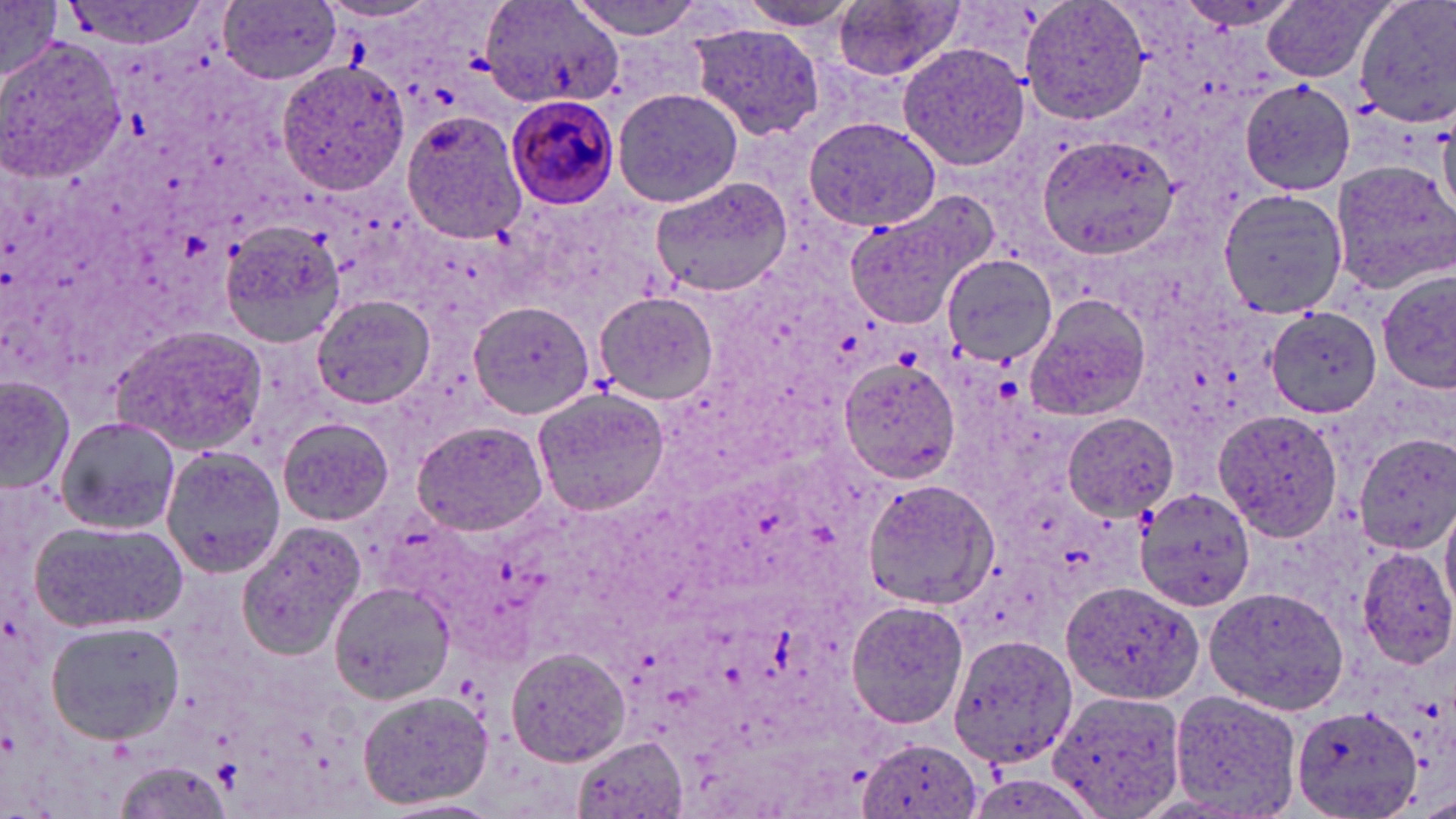
Summary:
  - Coordinate format: approximate bounding boxes as (x1,y1)-(x2,y2) corner pairs in pixels
  - Plasmodium malariae-infected red blood cell locations: (504,93)-(619,209)
  - Platelet locations: (211,761)-(239,790)
  - Uninfected red blood cell locations: (568,0)-(713,39), (732,0)-(867,29), (1021,0)-(1151,127), (1263,0)-(1389,83), (1352,0)-(1456,131), (55,1)-(212,48), (219,1)-(342,86), (2,2)-(63,82), (316,2)-(446,25), (484,2)-(623,107), (831,2)-(965,82), (684,23)-(829,140), (1,36)-(128,181), (898,42)-(1030,171), (275,59)-(408,195), (1240,79)-(1355,195), (611,86)-(746,209), (401,111)-(527,244), (799,115)-(944,234), (1032,134)-(1183,262), (1329,159)-(1456,290), (648,176)-(793,300), (1218,188)-(1349,319), (842,193)-(989,327), (218,220)-(348,347), (942,253)-(1058,366), (1377,271)-(1455,392), (593,290)-(720,406), (1024,292)-(1152,422), (311,294)-(436,411), (470,303)-(594,419), (1266,307)-(1383,417), (110,323)-(269,456), (837,357)-(961,485), (0,376)-(75,494), (531,384)-(670,520), (1216,410)-(1344,544), (1064,414)-(1178,520), (55,416)-(182,534), (277,416)-(395,526), (411,420)-(549,536), (1355,434)-(1455,555), (160,447)-(286,578), (866,480)-(994,611), (1136,489)-(1256,611), (1441,502)-(1456,617), (29,518)-(188,635), (236,520)-(368,659), (1355,546)-(1456,669), (329,579)-(453,704), (1059,583)-(1205,705), (1205,586)-(1353,715), (846,599)-(970,730), (45,621)-(187,745), (948,635)-(1077,771), (505,646)-(633,768), (357,687)-(494,811), (1165,688)-(1302,819), (1047,690)-(1185,819), (1291,705)-(1422,819), (572,735)-(688,817), (856,736)-(984,819), (110,761)-(235,818), (377,798)-(502,818)
  - Slide-level diagnosis: Plasmodium malariae
  - Field of view: one of a larger specimen
  - Preparation: thin blood film
  - Image size: 1456×819 pixels
  - Modality: optical microscopy
  - Magnification: 1000x
  - Stain: May-Grünwald-Giemsa